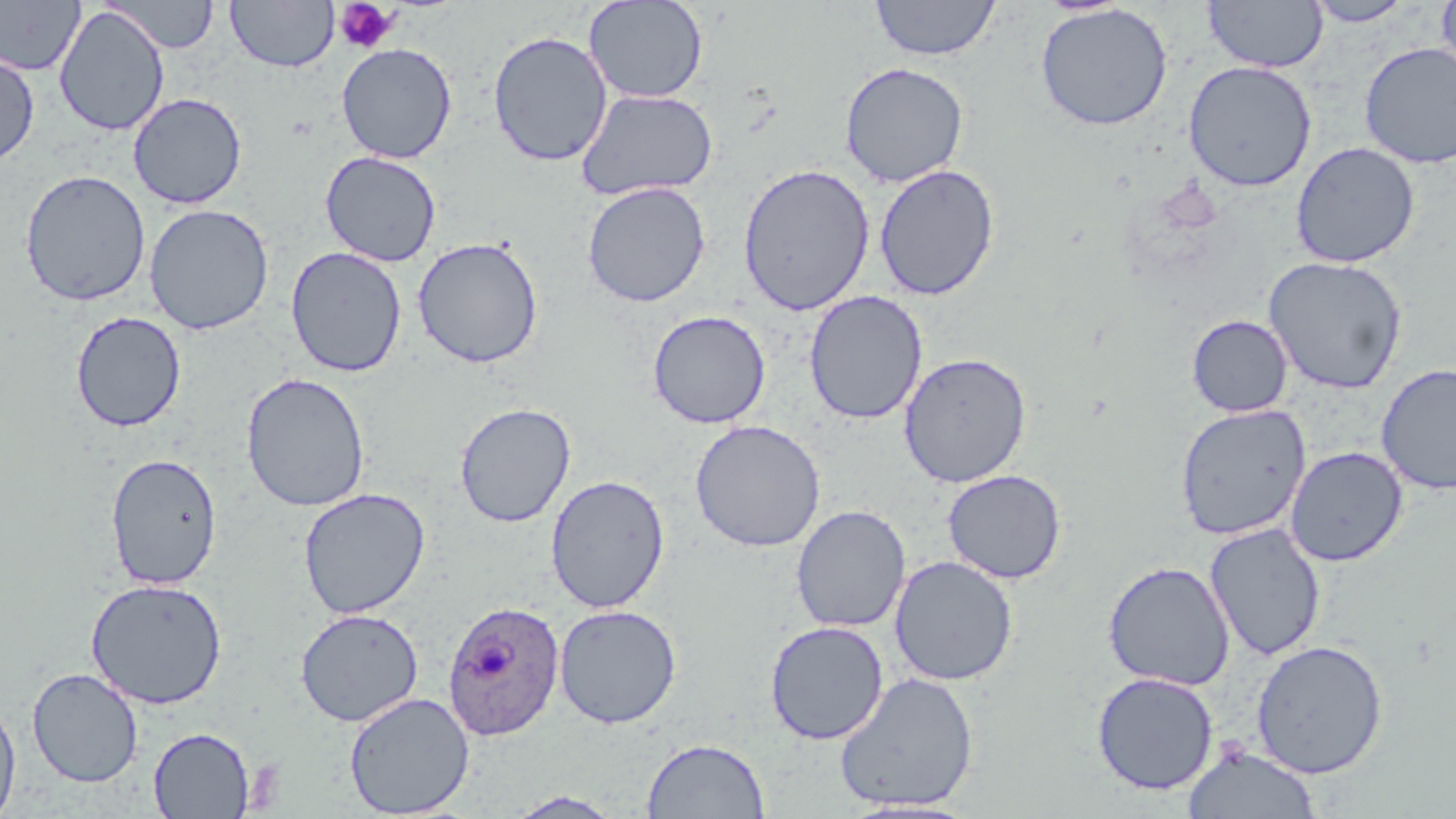

Summary:
  - Coordinate format: approximate bounding boxes as (x1, y1, x2, y2) in pixels
  - Uninfected red blood cell locations: (0, 0, 85, 76), (226, 0, 338, 73), (583, 0, 709, 104), (870, 0, 1001, 61), (1203, 0, 1328, 73), (1435, 0, 1456, 82), (105, 1, 220, 54), (1304, 1, 1415, 27), (1035, 4, 1173, 131), (54, 5, 170, 136), (487, 30, 613, 167), (336, 42, 457, 163), (1358, 42, 1456, 168), (0, 52, 39, 166), (1183, 60, 1317, 192), (840, 62, 969, 187), (577, 89, 717, 201), (128, 92, 247, 209), (1291, 141, 1420, 268), (320, 151, 441, 267), (737, 163, 875, 316), (873, 164, 1000, 301), (19, 169, 151, 307), (582, 182, 711, 307), (144, 203, 275, 335), (412, 236, 544, 369), (285, 246, 407, 378), (1263, 256, 1408, 394), (804, 290, 928, 424), (647, 309, 771, 429), (71, 310, 187, 432), (1186, 314, 1293, 417), (898, 352, 1032, 488), (1376, 363, 1456, 495), (241, 372, 371, 511), (454, 402, 576, 527), (1175, 403, 1312, 540), (690, 419, 826, 552), (1285, 446, 1408, 566), (106, 453, 222, 590), (942, 469, 1067, 584), (545, 474, 670, 613), (298, 488, 431, 619), (791, 505, 911, 633), (1204, 523, 1327, 662), (889, 555, 1018, 686), (1102, 560, 1236, 691), (86, 578, 228, 709), (554, 604, 682, 729), (295, 608, 424, 727), (765, 621, 888, 744), (1251, 639, 1388, 778), (27, 668, 143, 787), (1091, 671, 1219, 795), (834, 672, 979, 812), (344, 692, 474, 818), (0, 695, 21, 819), (148, 727, 255, 818), (641, 737, 770, 819), (1183, 744, 1322, 818), (504, 791, 626, 818)
  - Plasmodium ovale-infected red blood cell locations: (442, 599, 564, 740)
  - Platelet locations: (334, 1, 398, 54)
  - Slide-level diagnosis: Plasmodium ovale
  - Image size: 1456×819 pixels
  - Preparation: thin blood film
  - Stain: May-Grünwald-Giemsa
  - Field of view: single
  - Magnification: 1000x
  - Modality: light microscopy